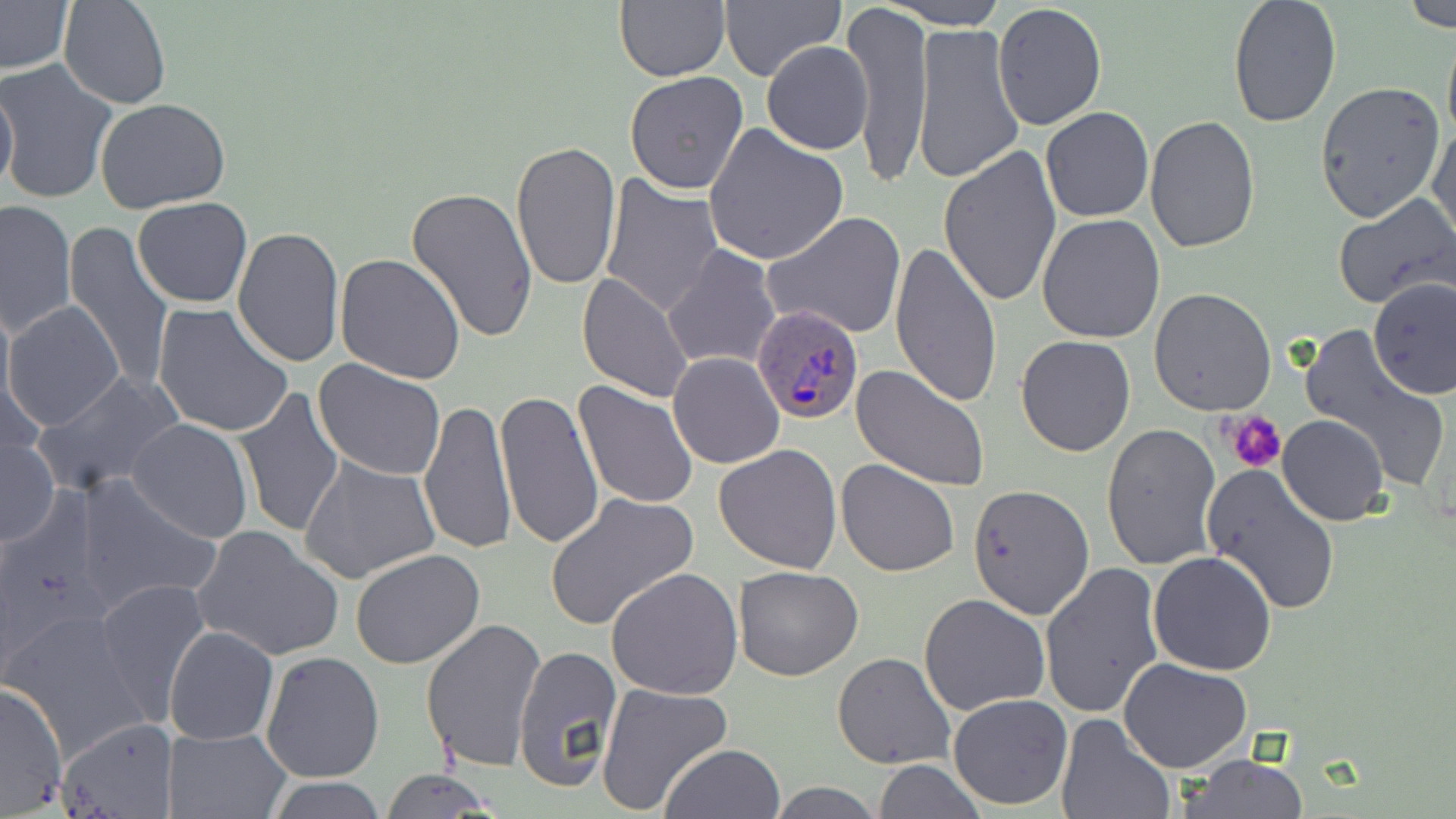
slide-level diagnosis = Plasmodium ovale
modality = light microscopy
magnification = 1000x
uninfected red blood cell locations = approximate bounding boxes as [x1, y1, x2, y2] in pixels: [60, 0, 171, 110], [613, 0, 729, 83], [720, 0, 843, 82], [0, 1, 74, 76], [889, 1, 1005, 29], [1227, 1, 1341, 127], [1397, 1, 1455, 31], [845, 4, 932, 184], [992, 4, 1108, 131], [913, 21, 1023, 185], [1441, 26, 1456, 151], [762, 39, 873, 156], [0, 61, 117, 205], [623, 71, 749, 196], [0, 76, 17, 200], [1314, 81, 1445, 224], [95, 98, 230, 213], [1041, 107, 1153, 222], [1146, 114, 1260, 255], [1427, 120, 1456, 248], [704, 124, 848, 267], [511, 140, 623, 294], [939, 145, 1062, 308], [600, 176, 726, 321], [407, 186, 538, 343], [1333, 195, 1456, 311], [133, 196, 254, 308], [0, 199, 76, 339], [763, 211, 907, 340], [1037, 213, 1166, 342], [62, 225, 174, 393], [231, 226, 343, 368], [889, 243, 1003, 410], [29, 244, 164, 470], [662, 246, 781, 371], [333, 254, 466, 385], [577, 273, 693, 403], [1368, 279, 1455, 400], [1150, 287, 1277, 415], [4, 300, 125, 433], [152, 302, 294, 438], [1297, 324, 1454, 496], [1015, 335, 1137, 457], [668, 352, 785, 469], [314, 359, 447, 479], [851, 364, 990, 491], [31, 372, 182, 500], [573, 381, 698, 509], [233, 388, 345, 537], [495, 392, 604, 551], [419, 399, 516, 554], [1277, 414, 1389, 526], [126, 418, 255, 542], [1102, 423, 1221, 570], [1, 432, 57, 548], [715, 443, 842, 575], [299, 455, 442, 586], [836, 460, 958, 577], [1202, 464, 1343, 617], [74, 474, 223, 617], [967, 482, 1095, 618], [546, 493, 700, 632], [192, 525, 343, 661], [350, 548, 485, 669], [1148, 552, 1278, 676], [1039, 562, 1163, 718], [608, 566, 745, 701], [732, 566, 862, 681], [96, 578, 211, 726], [919, 593, 1051, 717], [4, 609, 156, 766], [420, 617, 546, 772], [164, 626, 278, 745], [513, 645, 621, 793], [261, 650, 385, 781], [833, 651, 957, 769], [1119, 658, 1253, 772], [596, 682, 733, 815], [0, 684, 69, 812], [948, 693, 1073, 809], [1055, 713, 1175, 819], [56, 717, 177, 817], [163, 726, 291, 818], [661, 744, 786, 819], [1177, 754, 1310, 819], [874, 759, 986, 818], [380, 768, 502, 818], [262, 778, 390, 818], [768, 780, 882, 819]
platelet locations = approximate bounding boxes as [x1, y1, x2, y2] in pixels: [1225, 410, 1287, 475]
Plasmodium ovale-infected red blood cell locations = approximate bounding boxes as [x1, y1, x2, y2] in pixels: [754, 304, 865, 423]
image size = 1456×819 pixels
stain = May-Grünwald-Giemsa
preparation = thin blood film
field of view = single